Locate and identify every blood parasite.
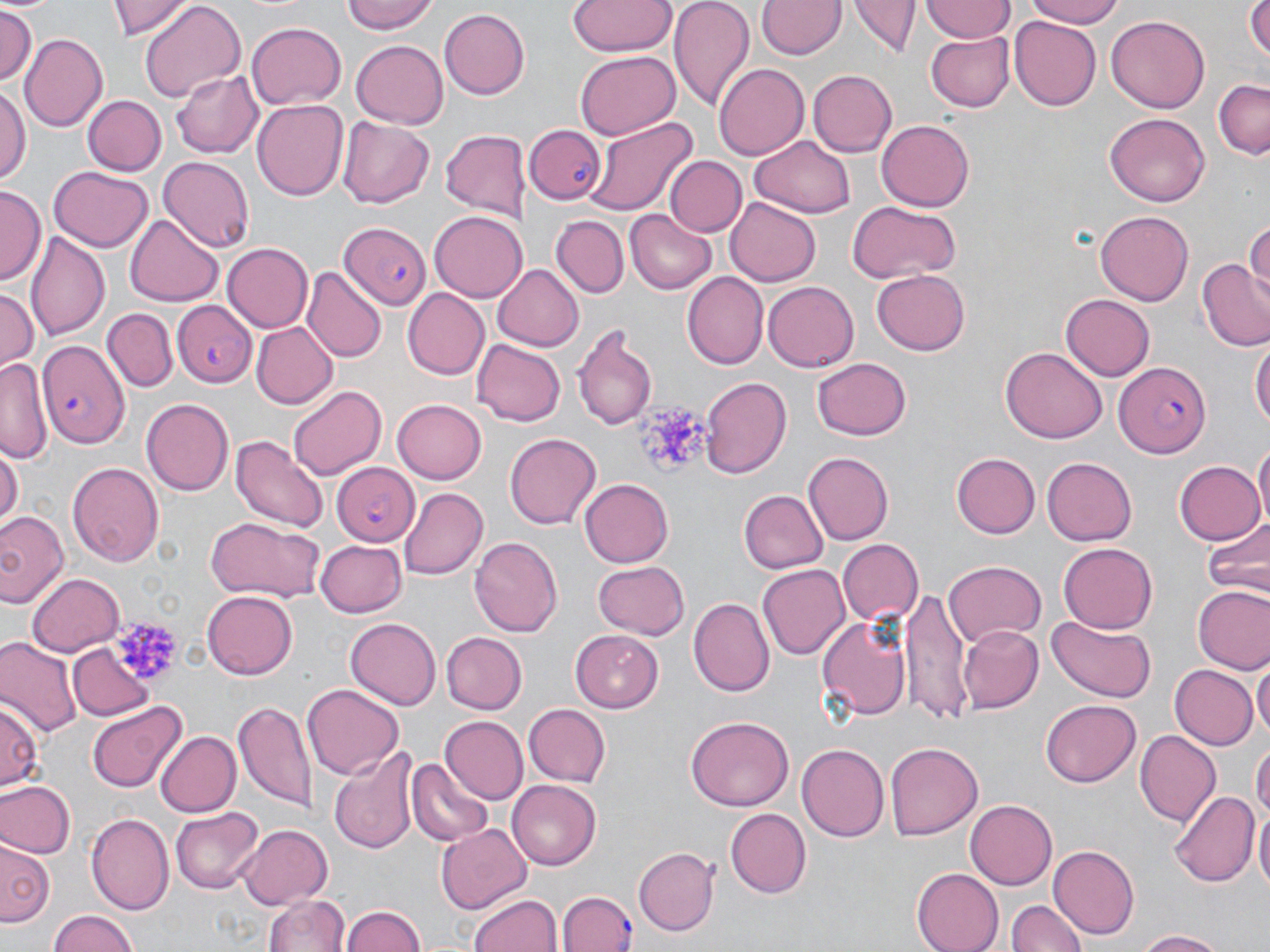
Approximate bounding boxes as (x1,y1)-(x2,y2) corner pairs in pixels.
Plasmodium falciparum-infected red blood cells: (530,126)-(604,204), (340,222)-(431,310), (173,300)-(257,387), (37,338)-(129,449), (1116,361)-(1213,458), (330,461)-(419,545), (556,891)-(636,952).
No Plasmodium ovale, Plasmodium malariae, Plasmodium vivax, Babesia divergens, or Trypanosoma brucei observed.

Summary:
  - Platelet locations: (639,398)-(708,474), (117,622)-(177,686)
  - Uninfected red blood cell locations: (108,0)-(196,39), (341,0)-(439,36), (569,0)-(677,56), (669,0)-(755,111), (757,0)-(845,60), (1023,0)-(1128,27), (1248,0)-(1269,67), (140,1)-(245,102), (922,1)-(1015,42), (851,2)-(918,59), (1,5)-(38,88), (440,7)-(530,99), (1009,15)-(1101,109), (1106,15)-(1210,113), (247,22)-(345,109), (926,32)-(1015,112), (20,33)-(108,131), (350,40)-(449,128), (575,49)-(681,140), (714,63)-(809,159), (808,70)-(896,158), (173,71)-(263,158), (1214,76)-(1270,159), (1,82)-(30,188), (80,94)-(166,177), (253,98)-(348,201), (1105,113)-(1210,207), (584,114)-(697,219), (337,117)-(436,207), (877,119)-(974,213), (440,126)-(526,219), (751,137)-(855,218), (665,155)-(747,237), (157,157)-(255,252), (47,166)-(153,254), (2,187)-(43,287), (725,196)-(820,285), (846,202)-(961,282), (429,210)-(529,301), (626,210)-(716,292), (1095,210)-(1195,306), (125,214)-(224,307), (552,216)-(628,297), (1246,223)-(1270,300), (25,231)-(110,341), (224,243)-(312,331), (1197,259)-(1270,352), (493,262)-(586,350), (301,266)-(385,365), (870,270)-(970,356), (681,272)-(768,369), (764,280)-(861,371), (0,288)-(38,374), (404,288)-(488,378), (1059,295)-(1155,381), (103,308)-(177,392), (251,322)-(336,408), (572,322)-(657,433), (471,337)-(566,425), (1250,337)-(1269,437), (1000,347)-(1106,444), (1,356)-(47,468), (810,357)-(913,441), (699,377)-(789,479), (288,384)-(388,481), (141,397)-(235,494), (392,398)-(485,481), (505,432)-(599,531), (231,433)-(328,532), (1254,439)-(1270,534), (0,444)-(21,532), (803,452)-(892,545), (951,453)-(1040,539), (1042,456)-(1138,545), (1173,460)-(1264,546), (68,461)-(165,567), (580,476)-(673,565), (398,488)-(488,581), (739,490)-(829,574), (0,509)-(68,610), (204,515)-(327,603), (1202,517)-(1269,597), (470,535)-(562,636), (314,539)-(405,615), (837,539)-(924,628), (1057,540)-(1156,631), (593,559)-(691,640), (944,559)-(1044,645), (757,564)-(849,660), (27,573)-(123,657), (1191,585)-(1270,675), (901,588)-(972,723), (201,589)-(295,680), (690,597)-(772,695), (817,611)-(912,724), (1047,613)-(1156,701), (345,617)-(442,708), (959,623)-(1044,714), (570,628)-(666,712), (441,632)-(527,713), (0,636)-(82,738), (67,643)-(160,723), (1253,654)-(1269,745), (1168,664)-(1258,751), (303,685)-(403,777), (2,696)-(42,791), (1040,700)-(1139,786), (86,701)-(187,793), (235,702)-(317,811), (522,702)-(608,784), (439,716)-(528,805), (686,716)-(793,812), (1136,729)-(1219,826), (155,730)-(240,817), (1253,739)-(1269,825), (886,742)-(983,840), (796,743)-(889,841), (330,747)-(419,853), (408,759)-(493,845), (1,779)-(76,858), (507,780)-(602,870), (1169,789)-(1257,887), (966,798)-(1057,889), (1255,806)-(1270,903), (169,807)-(262,896), (724,808)-(811,898), (87,812)-(175,912), (436,823)-(532,915), (234,824)-(333,910), (1,841)-(56,929), (1048,845)-(1139,937), (634,848)-(719,937), (912,869)-(1002,951), (264,893)-(351,952), (470,893)-(562,952), (1007,898)-(1085,952), (340,903)-(429,952), (46,909)-(142,952), (1132,929)-(1233,951)
  - Slide-level diagnosis: Plasmodium falciparum
  - Magnification: 1000x
  - Image size: 1270×952 pixels
  - Preparation: thin blood smear
  - Stain: May-Grünwald-Giemsa
  - Field of view: one of a larger specimen
  - Modality: light microscopy